Report the malaria status.
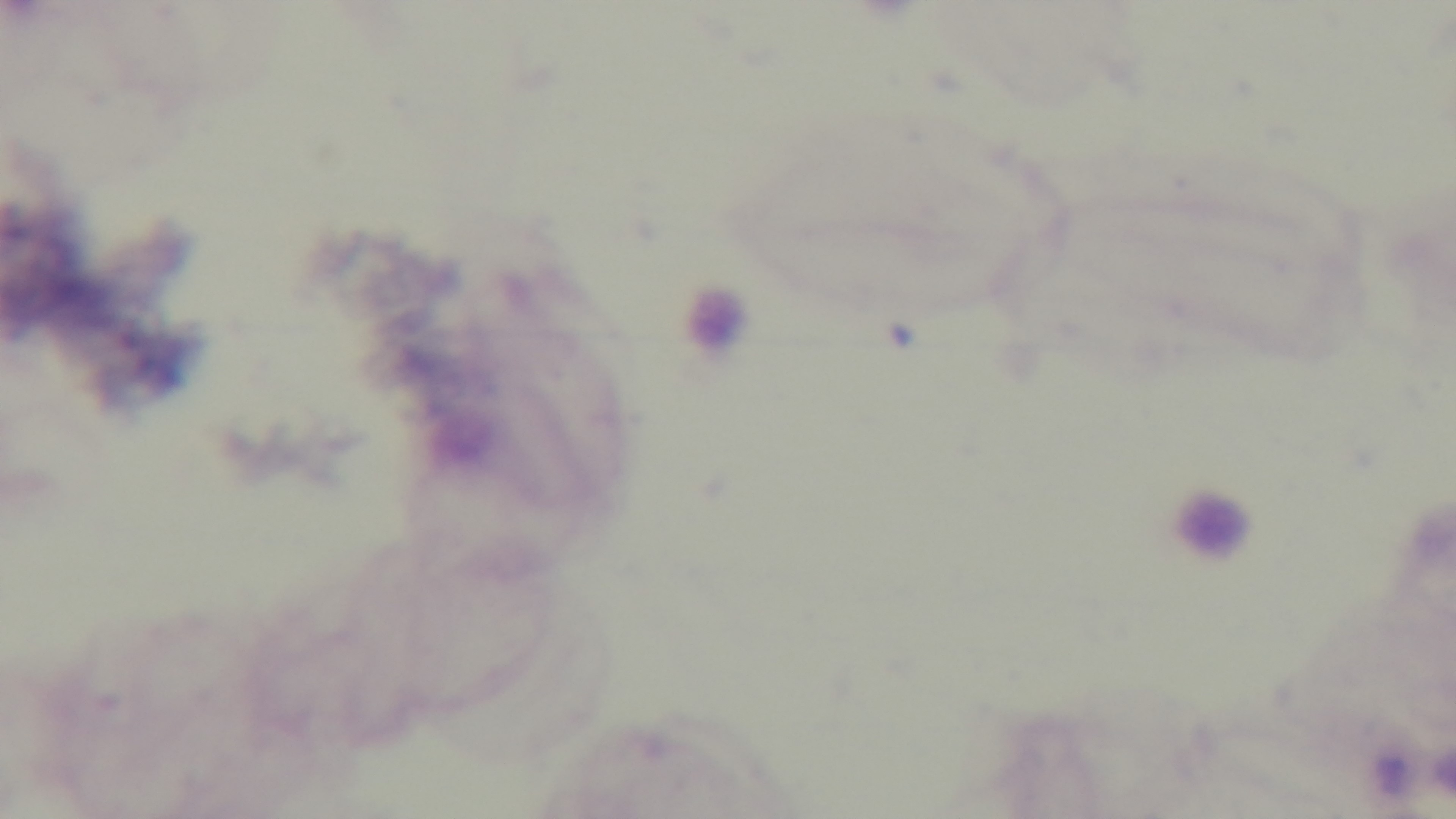
Negative.

Summary:
  - Field of view: one from the slide
  - Modality: light microscopy
  - Preparation: thick blood film
  - Objective: 100x oil immersion
  - Stain: Giemsa
  - Capture: mounted 4K digital camera